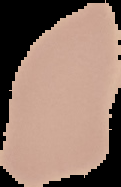

result = negative for malaria parasites
preparation = thin blood film
image type = segmented cell region on a black background
image size = 121×187 pixels